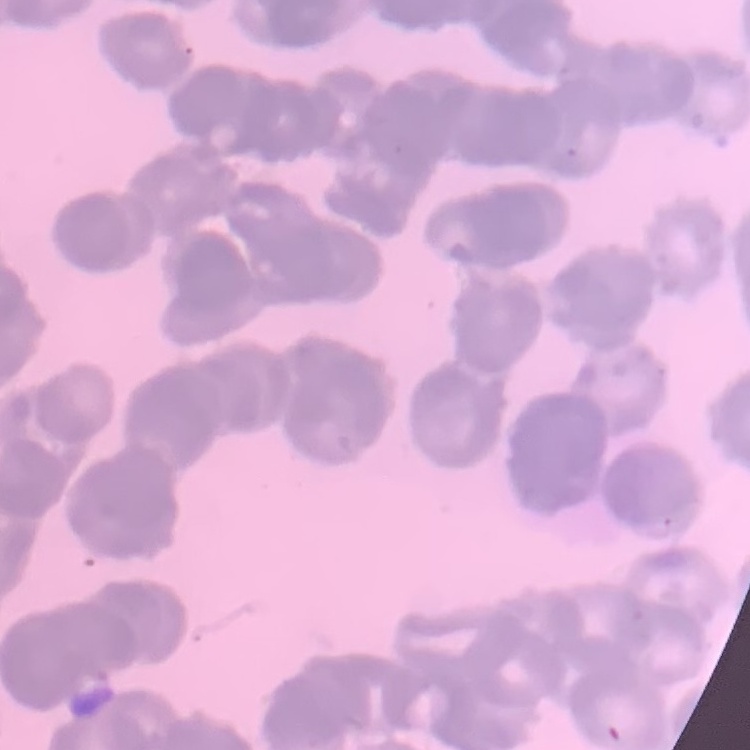

Summary:
  - Erythrocyte morphology: rouleaux formation
  - Image type: one tile cut from a larger photomicrograph
  - Stain: Field's or Giemsa
  - Preparation: thin peripheral smear